State which parasite is depicted.
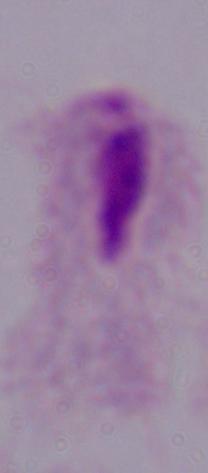

This is a trichomonad.

Summary:
  - Modality: micrograph
  - Magnification: 1000x